Assess this cell for malaria.
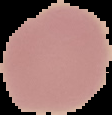
Uninfected.

image type = segmented cell region with the area outside set to black
preparation = thin blood film
image size = 112×115 pixels